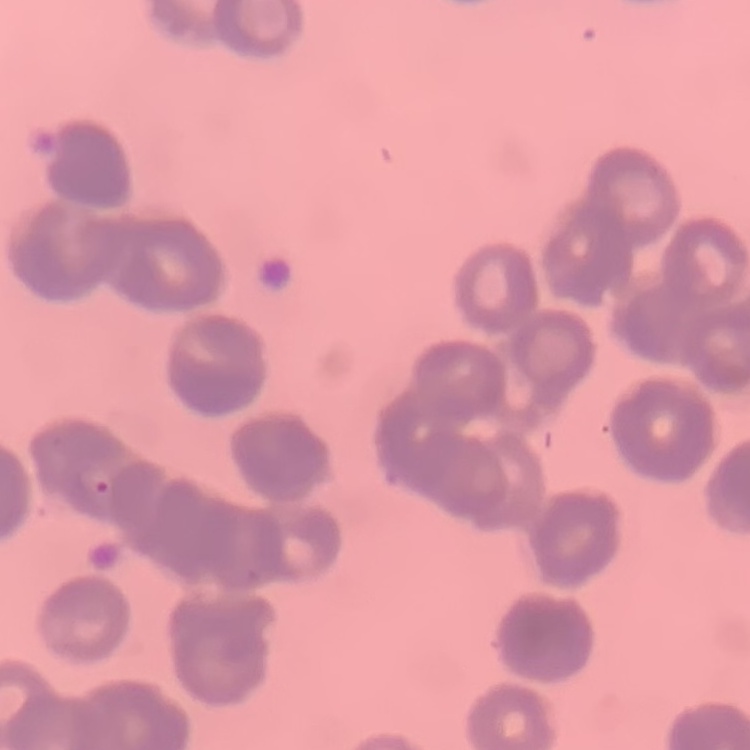

erythrocyte morphology = rouleaux formation
image type = one tile cut from a larger photomicrograph
stain = Field's or Giemsa
preparation = thin blood smear